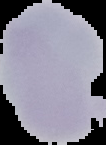

preparation: thin blood smear
image_type: cell region segmented out of the field of view; surrounding area masked to black
malaria_status: uninfected
image_size: 106×145 pixels